Classify this cell by malaria status.
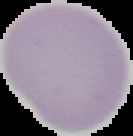
It is uninfected.

{
  "preparation": "thin blood smear",
  "image_size": "133×136 pixels",
  "image_type": "segmented cell region with the area outside set to black"
}